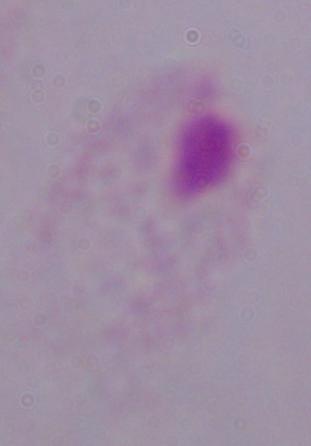
A trichomonad is seen. Micrograph. 1000x magnification.